Identify the parasite.
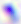
This is Toxoplasma gondii.

Captured at 400x magnification. Photomicrograph.